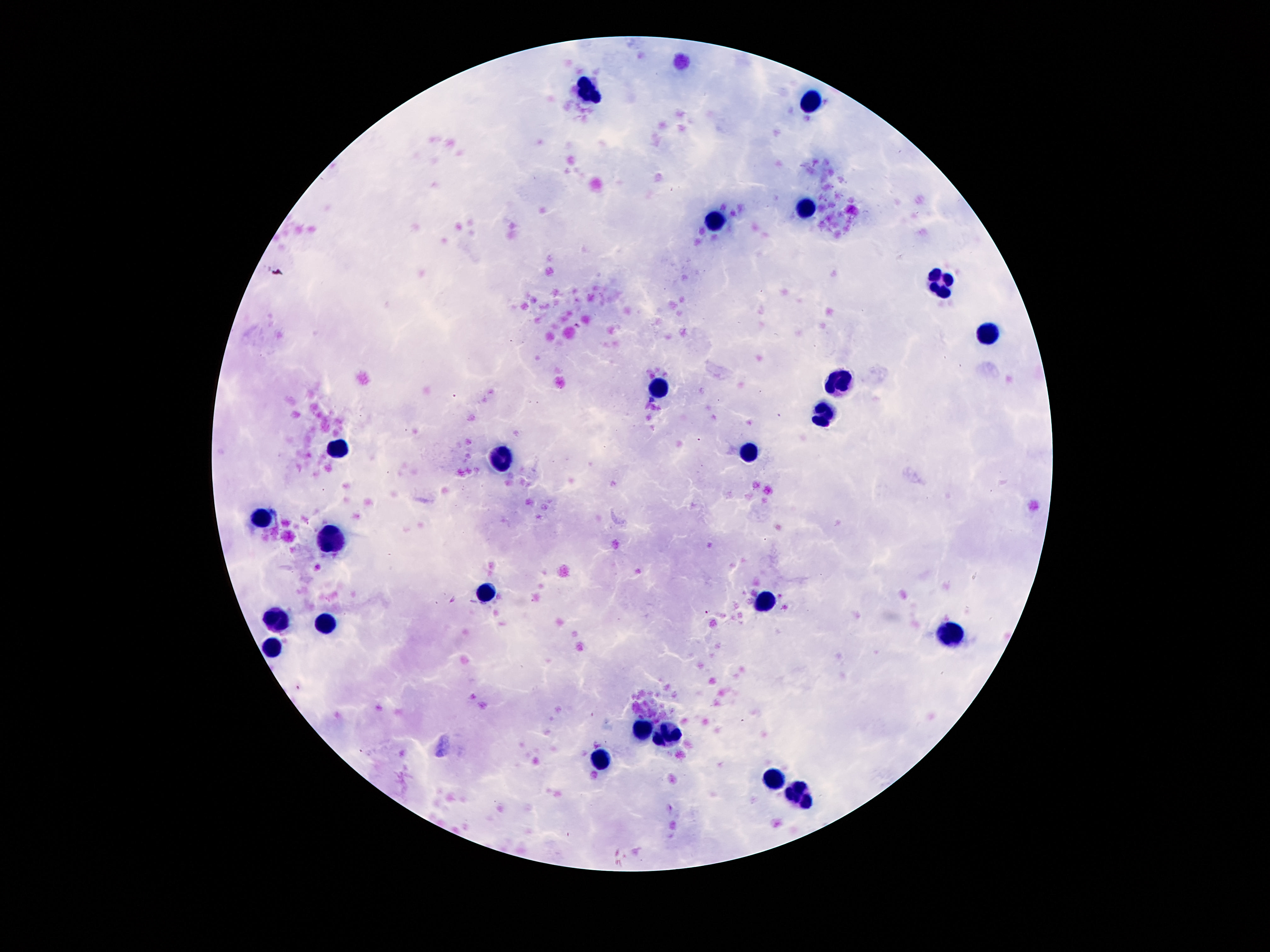

Approximate centers as [x, y] in pixels. Leukocyte locations: [589, 91], [810, 99], [803, 207], [717, 219], [942, 282], [988, 335], [843, 380], [656, 389], [824, 415], [335, 450], [747, 455], [501, 459], [260, 518], [333, 536], [486, 591], [764, 602], [276, 618], [327, 623], [952, 636], [272, 646], [644, 728], [667, 732], [598, 761], [774, 778], [799, 793]. Image is 1270×952 pixels. Giemsa stain. 100x magnification. Patient malaria status: not infected. Single field of view. Photographed through the microscope eyepiece with a smartphone camera. Thick blood film.